Name the cell type shown.
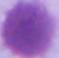
An erythrocyte.

Summary:
  - Magnification: 1000x
  - Modality: micrograph